Locate leukocytes (white blood cells).
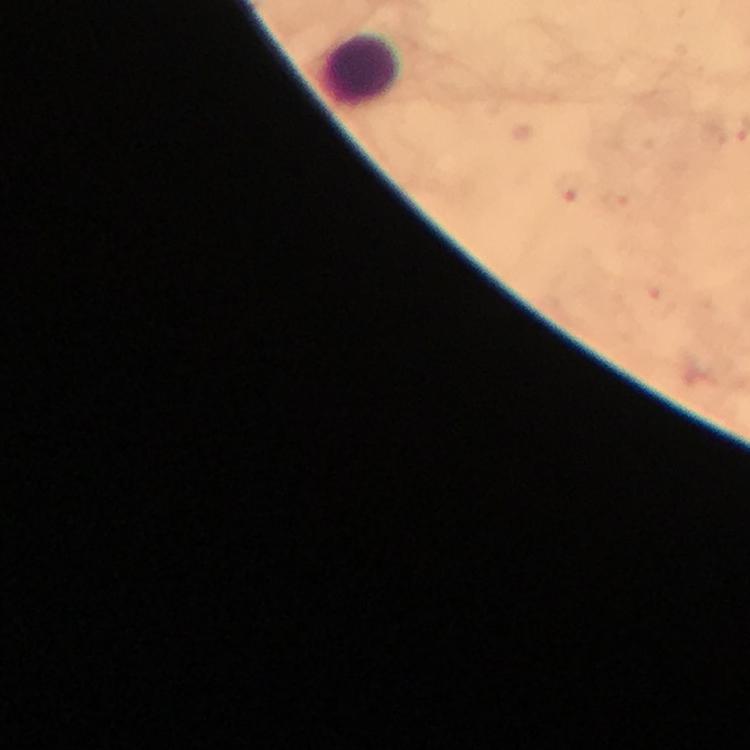
Approximate object centers, in pixels from the top-left corner.
Leukocytes: (x=359, y=68).

cropped from = one field of view
preparation = thick smear
image size = 750×750 pixels
magnification = 100x
stain = Giemsa
context = from a malaria diagnostic workup
capture = smartphone camera through the microscope
malaria parasites = none detected
immersion oil = applied